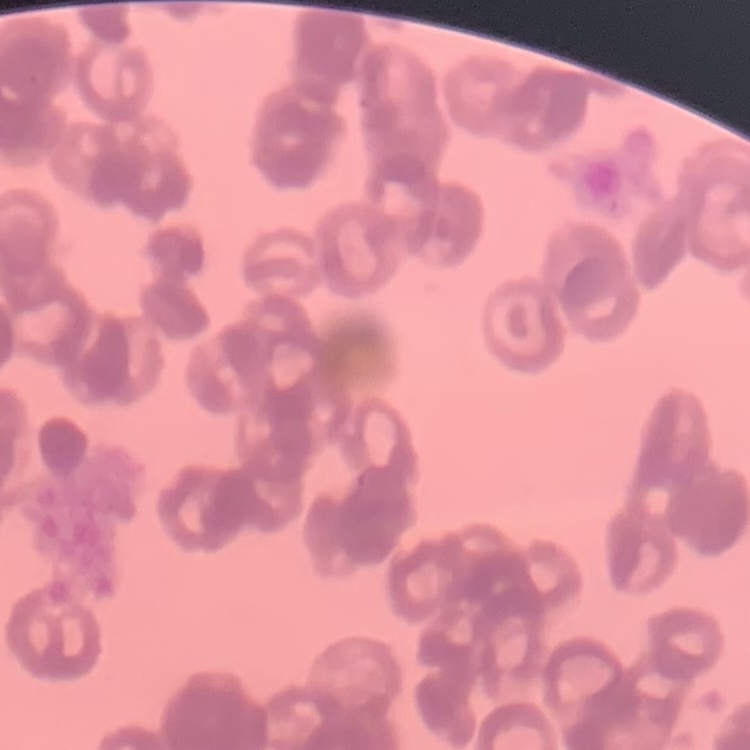
Summary:
  - Red blood cell morphology: rouleaux formation
  - Stain: Field's or Giemsa
  - Image type: one tile cut from a larger photomicrograph
  - Preparation: thin blood film